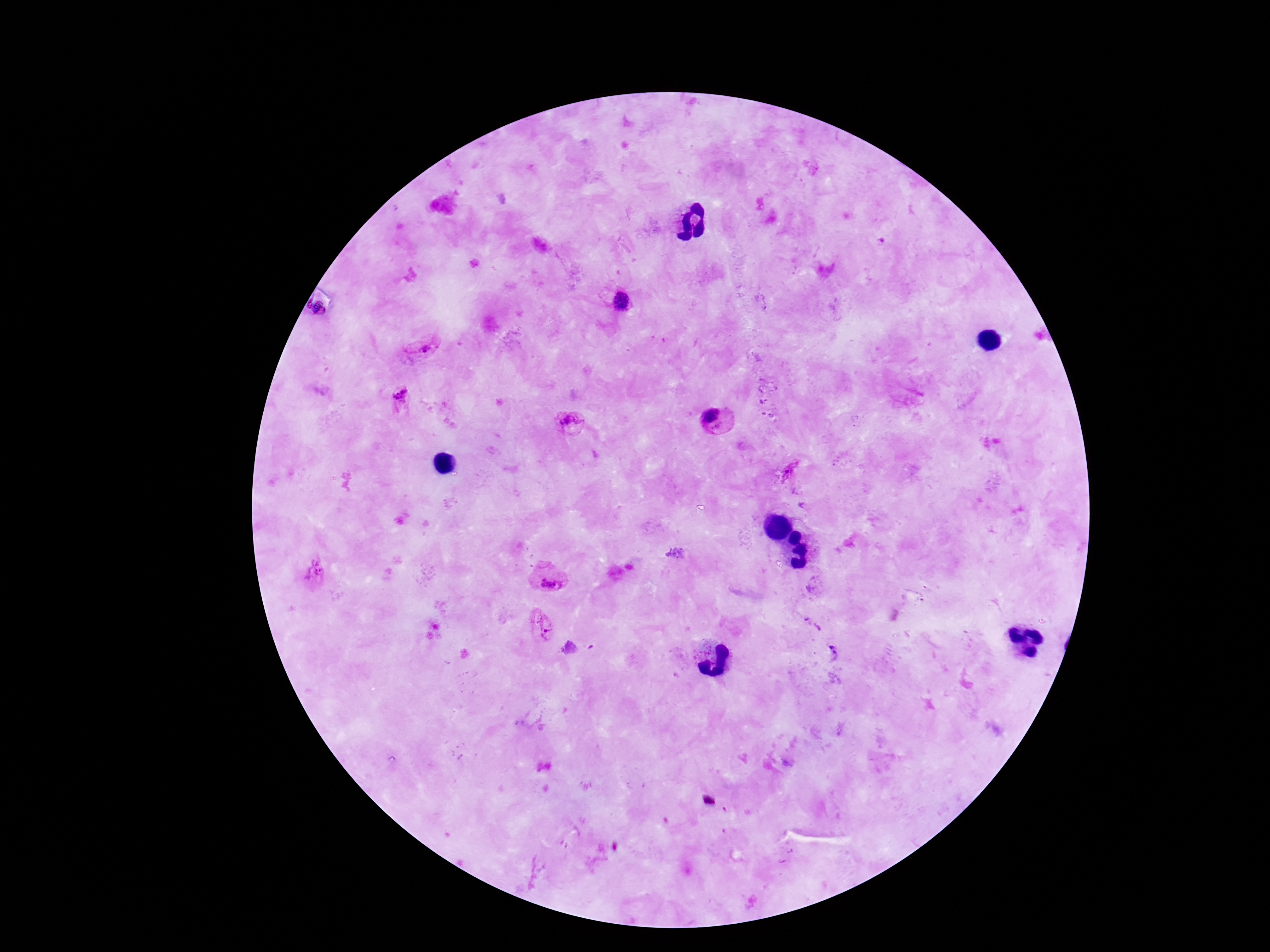

Approximate centers as {x, y} in pixels.
Summary:
  - Plasmodium parasite locations: {621, 302}, {422, 346}, {401, 397}, {713, 418}, {570, 423}, {790, 474}, {315, 571}, {551, 582}, {546, 632}, {833, 654}
  - Magnification: 100x
  - Preparation: thick peripheral-blood smear
  - Stain: Giemsa
  - Field of view: one from this slide
  - Capture: smartphone camera through the microscope eyepiece
  - Image size: 1270×952 pixels
  - Patient malaria status: infected